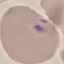
Malaria status: uninfected. Photographed with a smartphone camera at the microscope eyepiece. Automatically extracted cell patch, resized to 64 × 64 pixels. Giemsa stain. Thin smear of blood.